Locate every blood parasite and identify its species.
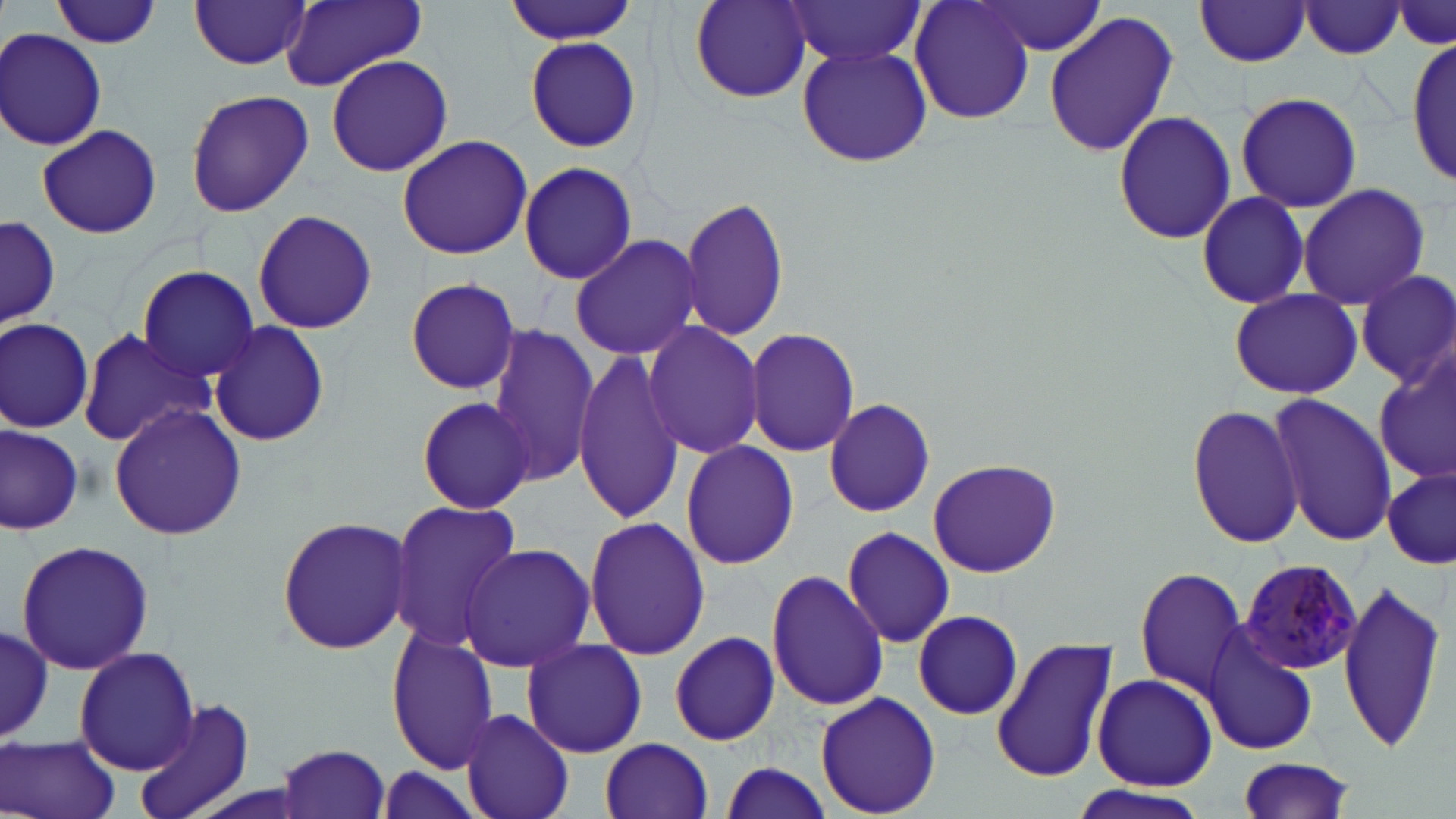
Approximate bounding boxes as (x1, y1, x2, y2) in pixels.
Plasmodium malariae-infected red blood cells: (1232, 554, 1362, 678).
No Plasmodium falciparum, Plasmodium ovale, Plasmodium vivax, Babesia divergens, or Trypanosoma brucei observed.

Uninfected red blood cell locations: (51, 0, 162, 49), (280, 0, 428, 91), (501, 0, 637, 48), (688, 0, 816, 104), (782, 0, 927, 69), (911, 0, 1034, 125), (1393, 0, 1455, 52), (188, 1, 314, 71), (974, 2, 1108, 58), (1193, 2, 1313, 67), (1297, 3, 1409, 60), (1043, 9, 1177, 161), (1, 28, 109, 152), (523, 33, 643, 155), (1408, 41, 1454, 184), (796, 44, 932, 168), (325, 54, 454, 177), (184, 89, 315, 217), (1236, 92, 1362, 211), (1112, 109, 1237, 247), (37, 124, 163, 239), (396, 134, 533, 260), (516, 162, 637, 285), (1295, 183, 1431, 311), (1194, 192, 1311, 309), (679, 194, 790, 342), (253, 208, 377, 335), (1, 215, 59, 331), (569, 233, 702, 360), (134, 263, 262, 382), (1355, 269, 1455, 387), (404, 278, 520, 395), (1229, 288, 1361, 399), (1, 316, 95, 434), (207, 319, 331, 448), (643, 320, 766, 460), (484, 325, 600, 484), (75, 326, 217, 447), (744, 327, 862, 458), (572, 349, 685, 525), (1374, 353, 1454, 483), (1268, 393, 1396, 547), (414, 394, 537, 514), (823, 396, 936, 518), (107, 402, 247, 539), (1186, 402, 1306, 549), (0, 425, 84, 533), (680, 440, 801, 570), (926, 460, 1061, 577), (1382, 467, 1455, 570), (389, 500, 521, 651), (274, 516, 414, 656), (583, 516, 710, 660), (841, 523, 955, 649), (15, 538, 155, 676), (459, 543, 593, 673), (766, 568, 887, 712), (1135, 568, 1246, 695), (1337, 575, 1446, 754), (912, 609, 1023, 719), (0, 618, 55, 748), (1201, 624, 1318, 756), (386, 627, 500, 775), (670, 631, 779, 747), (991, 636, 1117, 784), (521, 638, 648, 758), (74, 646, 199, 775), (1091, 672, 1218, 790), (813, 691, 942, 816), (131, 697, 254, 819), (461, 708, 573, 819), (2, 734, 122, 819), (600, 737, 713, 819), (276, 743, 393, 817), (1235, 755, 1359, 819), (716, 761, 834, 819), (374, 764, 487, 819), (1066, 782, 1212, 818). Slide-level diagnosis: Plasmodium malariae. May-Grünwald-Giemsa stain. Light microscopy. Thin blood film. Single field of view. Image is 1456×819 pixels. 1000x magnification.